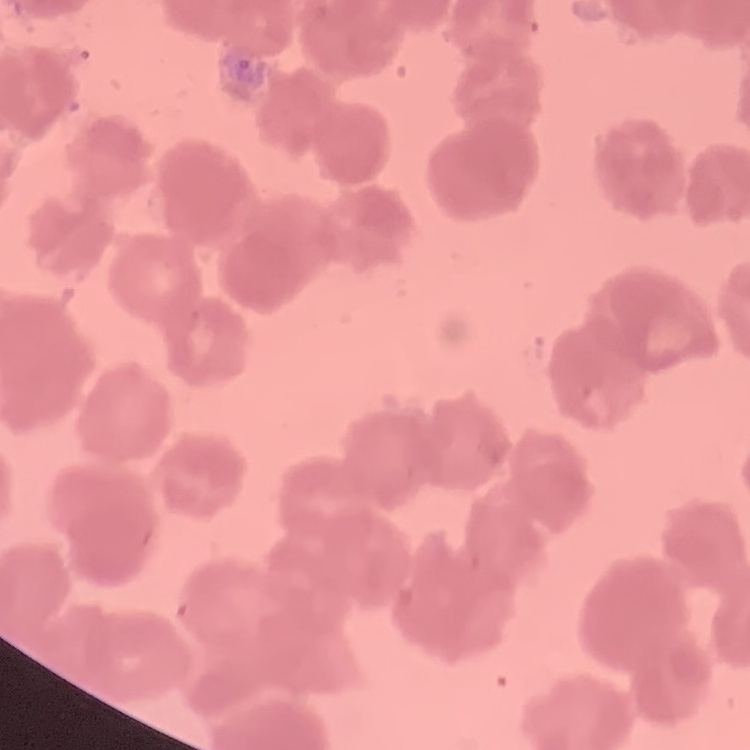
erythrocyte morphology = rouleaux formation
preparation = thin peripheral smear
image type = one tile cut from a larger photomicrograph
stain = Field's or Giemsa